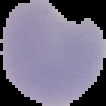

Summary:
  - Image size: 106×106 pixels
  - Image type: segmented cell region on a black background
  - Preparation: thin blood smear
  - Malaria status: parasitized